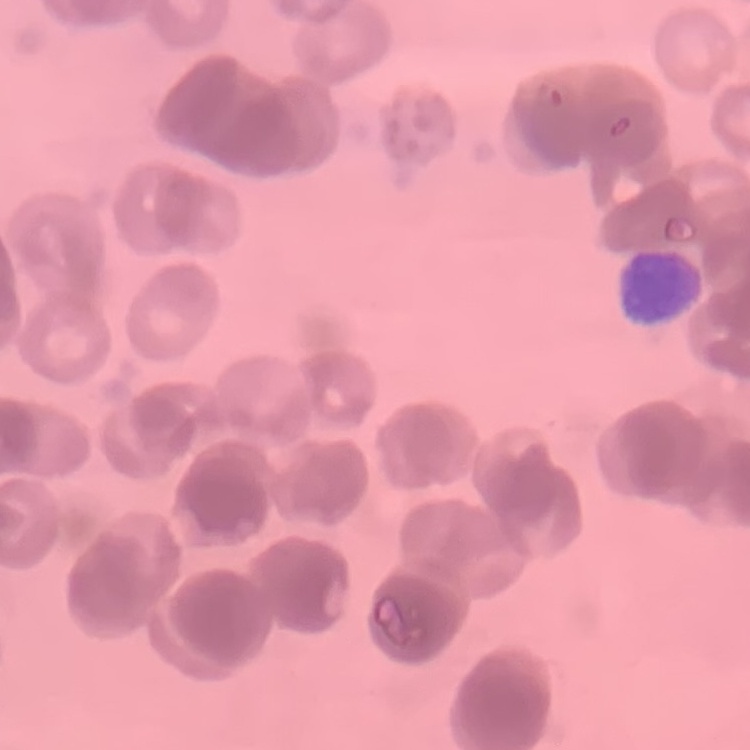
The erythrocytes exhibit rouleaux formation. Stained with either Field's or Giemsa. One tile cut from a larger photomicrograph. Thin blood film.